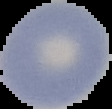

Summary:
  - Preparation: thin blood film
  - Image type: cell region segmented out of the field of view; surrounding area masked to black
  - Image size: 112×109 pixels
  - Result: negative for Plasmodium parasites